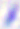
modality = photomicrograph
magnification = 400x
identification = Toxoplasma gondii